Assess for malaria.
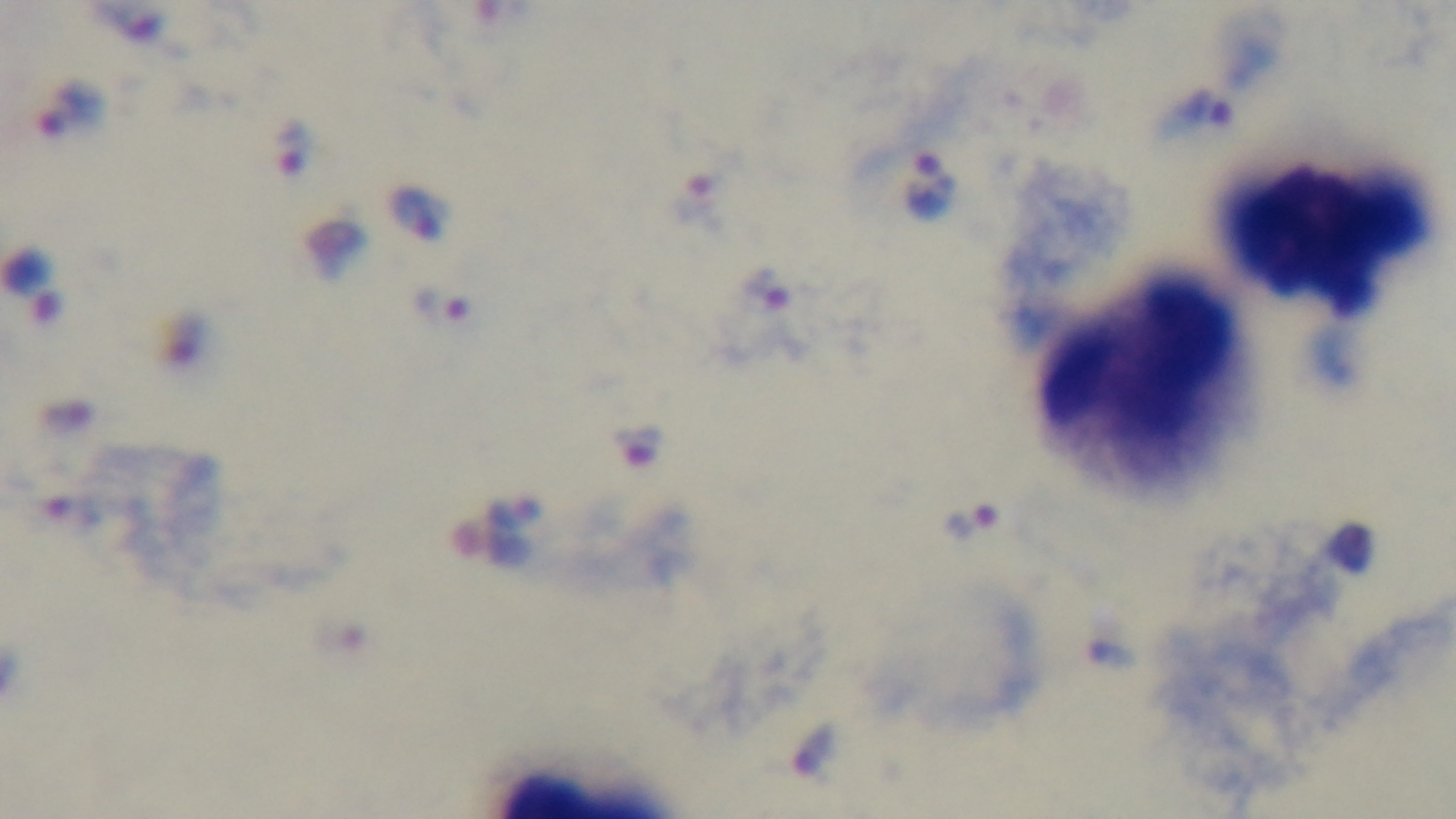

Positive.

Summary:
  - Modality: light microscopy
  - Stain: Giemsa
  - Objective: 100x oil immersion
  - Preparation: thick blood film
  - Capture: mounted 4K digital camera
  - Field of view: one from the slide